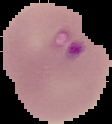
Summary:
  - Preparation: thin blood film
  - Image type: cell region segmented out of the field of view; surrounding area masked to black
  - Image size: 112×124 pixels
  - Malaria status: parasitized